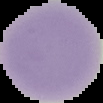 Image is 103×103 pixels. From a thin blood smear. Malaria status: uninfected. The area outside the segmented cell region is set to black.